Report the malaria status of this cell.
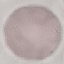

It is uninfected.

Giemsa-stained preparation. Thin blood smear. Cell patch, automatically extracted from a larger field of view and resized to 64 × 64 pixels. Photographed with a smartphone camera at the microscope eyepiece.